Report the malaria status of this cell.
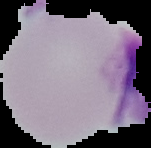

It is uninfected.

image size = 151×148 pixels
preparation = thin blood smear
image type = cell region segmented out of the field of view; surrounding area masked to black